Identify the parasite.
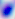

Toxoplasma gondii.

magnification = 400x
modality = micrograph